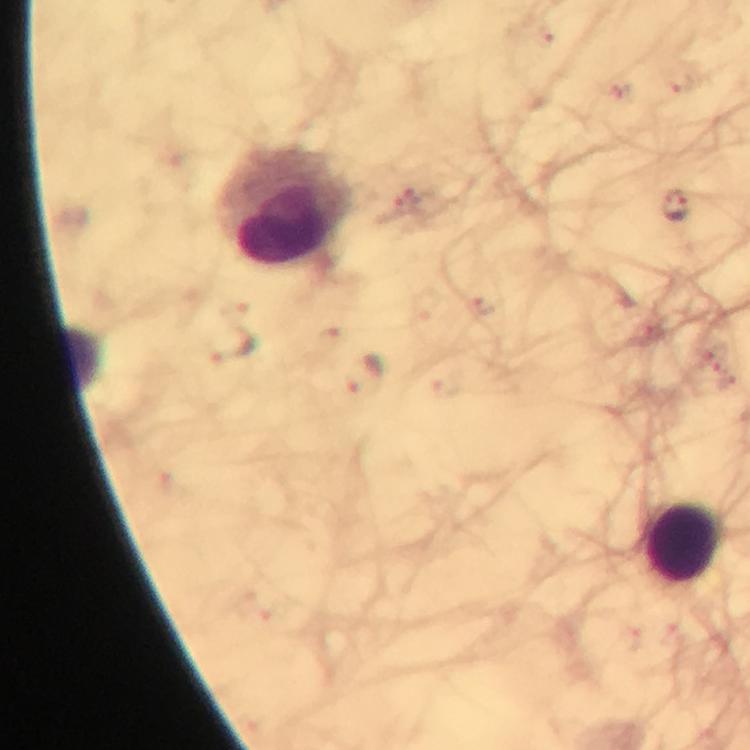

Approximate object centers, in pixels from the top-left corner.
Summary:
  - Malaria parasite locations: (x=675, y=205), (x=232, y=346), (x=367, y=377)
  - Leukocyte locations: (x=288, y=210), (x=683, y=544)
  - Stain: Giemsa
  - Cropped from: one field of view
  - Magnification: 100x
  - Capture: smartphone mounted on the microscope
  - Context: from a malaria diagnostic workup
  - Immersion oil: used
  - Preparation: thick blood smear
  - Image size: 750×750 pixels